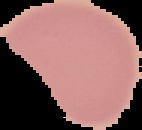 From a thin blood film. Cell region segmented out of the field of view; the surrounding area is masked to black. Result: no Plasmodium parasites detected. Image is 142×130 pixels.